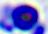

Summary:
  - Magnification: 400x
  - Modality: micrograph
  - Identification: white blood cell